Name the blood parasite species.
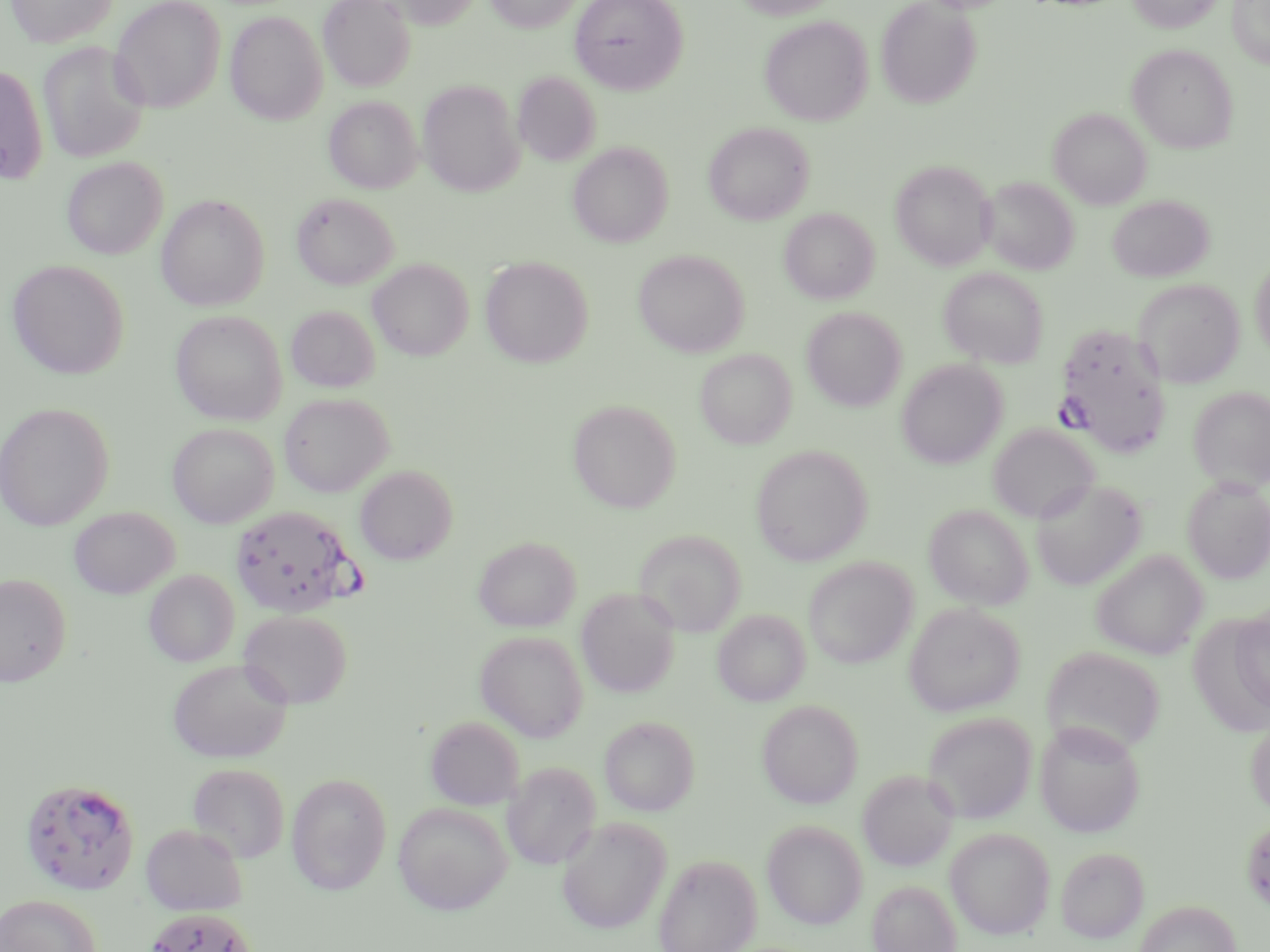

Plasmodium falciparum.

Approximate bounding boxes as (x1, y1, x2, y2) in pixels. Plasmodium falciparum-infected red blood cell locations: (1052, 323, 1172, 458), (230, 505, 360, 618), (20, 778, 140, 895), (144, 908, 258, 952). Uninfected red blood cell locations: (5, 0, 118, 49), (110, 0, 225, 113), (318, 0, 416, 92), (381, 0, 481, 29), (484, 0, 583, 33), (570, 0, 688, 94), (734, 0, 841, 19), (875, 0, 982, 108), (1127, 0, 1223, 33), (1227, 0, 1270, 68), (225, 11, 328, 125), (759, 15, 873, 126), (38, 41, 151, 164), (1128, 44, 1239, 154), (0, 64, 48, 185), (513, 72, 601, 166), (417, 79, 524, 197), (324, 96, 422, 193), (1048, 108, 1151, 209), (704, 122, 814, 225), (568, 142, 673, 248), (62, 157, 167, 259), (890, 160, 994, 269), (982, 176, 1079, 274), (291, 192, 398, 290), (156, 194, 270, 311), (1108, 195, 1213, 282), (779, 207, 879, 304), (633, 249, 749, 357), (480, 256, 594, 368), (1250, 257, 1270, 359), (7, 259, 130, 380), (368, 259, 474, 360), (939, 267, 1048, 368), (1134, 279, 1244, 388), (286, 306, 380, 393), (801, 306, 906, 411), (170, 309, 288, 425), (695, 348, 796, 449), (896, 359, 1007, 469), (1189, 386, 1270, 491), (279, 392, 394, 497), (568, 399, 681, 513), (0, 402, 115, 531), (167, 423, 279, 528), (988, 423, 1099, 524), (751, 444, 873, 566), (355, 465, 458, 565), (1182, 477, 1270, 583), (1031, 479, 1147, 590), (924, 504, 1034, 609), (69, 506, 179, 599), (634, 529, 747, 636), (474, 535, 581, 632), (1092, 548, 1208, 659), (803, 556, 918, 669), (144, 569, 239, 666), (0, 573, 71, 686), (576, 587, 680, 698), (903, 603, 1024, 717), (1231, 605, 1270, 717), (238, 609, 352, 708), (713, 609, 810, 706), (475, 630, 588, 742), (1041, 645, 1166, 756), (167, 658, 293, 764), (757, 699, 863, 808), (922, 711, 1037, 824), (1246, 713, 1270, 820), (424, 716, 525, 810), (599, 716, 700, 816), (1034, 720, 1146, 838), (502, 761, 601, 870), (187, 762, 291, 863), (857, 768, 958, 871), (286, 772, 392, 895), (393, 801, 512, 915), (1241, 816, 1270, 914), (557, 817, 671, 934), (761, 819, 869, 930), (141, 822, 248, 916), (944, 827, 1055, 939), (1056, 846, 1149, 943), (654, 854, 761, 952), (867, 880, 961, 952), (0, 894, 100, 952), (1134, 899, 1241, 952). May-Grünwald-Giemsa stain. 1000x magnification. Single field of view. Thin blood smear. Image is 1270×952 pixels. Optical microscopy.